State which parasite is depicted.
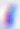
This is Toxoplasma gondii.

Photomicrograph. Captured at 400x magnification.